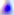
Toxoplasma gondii is shown. 400x magnification. Photomicrograph.